Assess this cell for malaria.
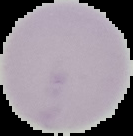
It is uninfected.

Summary:
  - Preparation: thin blood smear
  - Image type: segmented cell region on a black background
  - Image size: 133×136 pixels